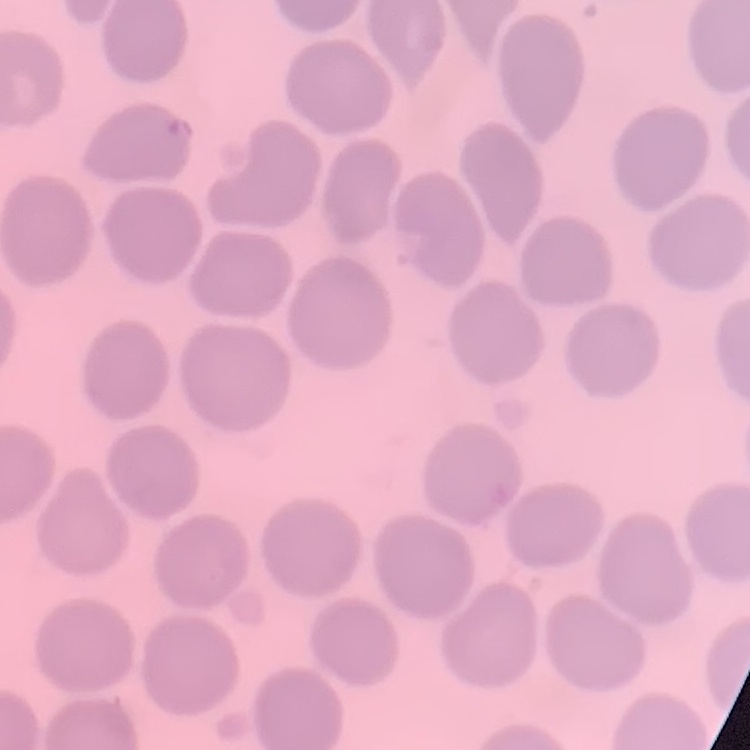
The erythrocytes show no rouleaux formation. Thin blood film. Field's or Giemsa stain. Square crop of a larger photomicrograph.